Classify this cell by malaria status.
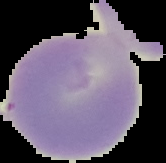

It is uninfected.

{
  "preparation": "thin blood smear",
  "image_size": "166×163 pixels",
  "image_type": "cell region segmented out of the field of view; surrounding area masked to black"
}